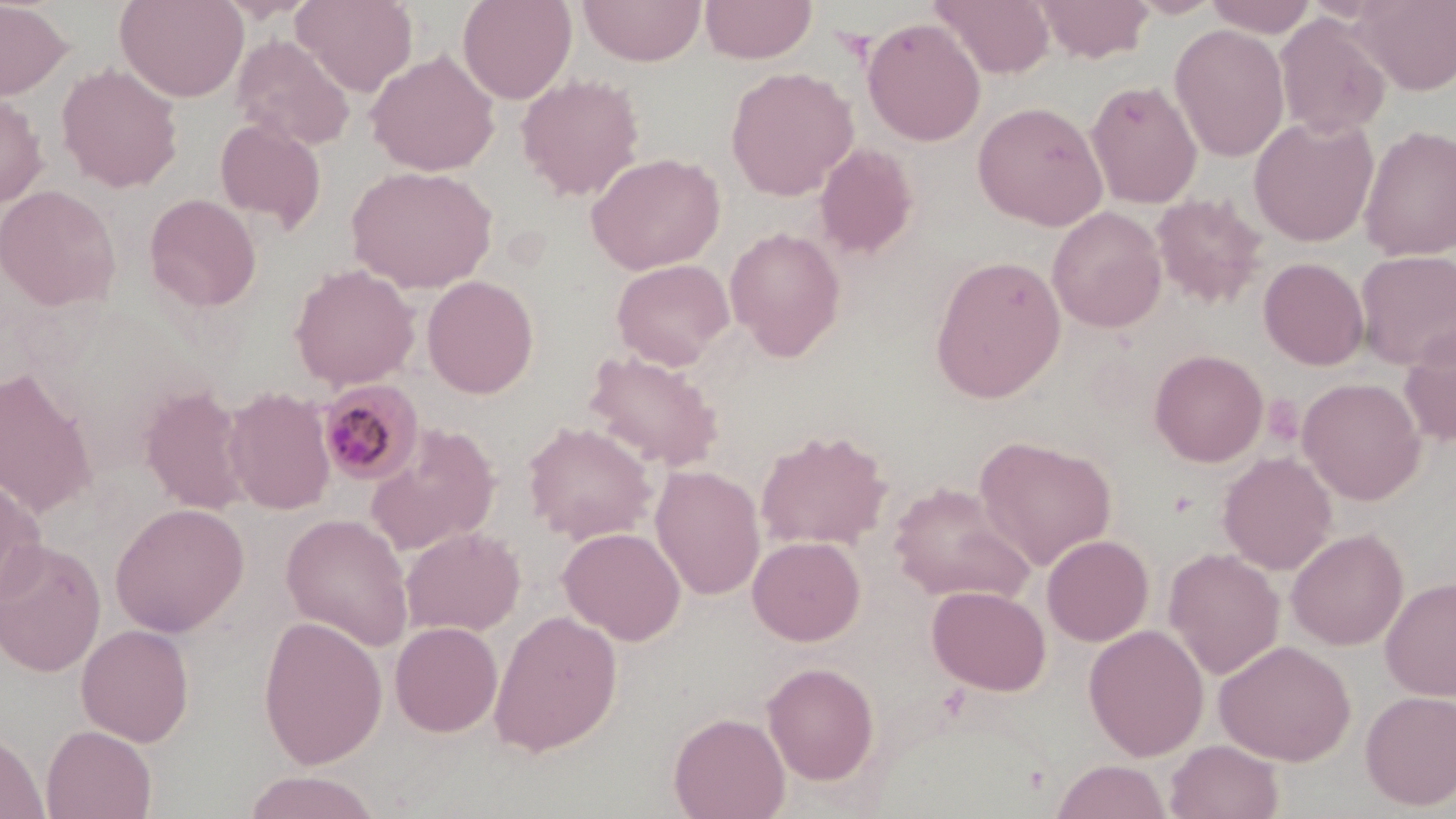 Approximate bounding boxes as (x1, y1, x2, y2) in pixels. Uninfected red blood cell locations: (0, 0, 75, 101), (115, 0, 248, 102), (291, 0, 418, 95), (457, 0, 576, 104), (699, 0, 817, 64), (931, 0, 1055, 79), (1034, 0, 1155, 63), (1127, 0, 1226, 19), (1203, 0, 1319, 37), (1353, 0, 1456, 95), (578, 1, 707, 66), (1274, 14, 1391, 139), (862, 17, 986, 147), (1169, 24, 1290, 162), (231, 34, 355, 151), (365, 49, 500, 176), (56, 63, 183, 193), (726, 66, 858, 200), (516, 74, 645, 200), (1086, 79, 1202, 208), (0, 91, 49, 209), (972, 101, 1108, 231), (1248, 114, 1379, 247), (215, 118, 326, 231), (1359, 124, 1456, 261), (815, 142, 919, 259), (586, 152, 725, 274), (346, 165, 498, 293), (0, 184, 122, 311), (1151, 192, 1268, 310), (144, 193, 262, 312), (1048, 206, 1167, 332), (724, 227, 846, 360), (1355, 250, 1456, 370), (930, 254, 1067, 403), (1258, 257, 1370, 371), (611, 258, 734, 369), (289, 264, 421, 391), (422, 275, 539, 399), (1399, 324, 1456, 447), (1149, 349, 1268, 467), (583, 351, 724, 471), (0, 367, 98, 517), (1297, 377, 1426, 505), (140, 386, 251, 514), (223, 386, 336, 515), (523, 422, 657, 543), (364, 423, 501, 555), (755, 429, 892, 551), (974, 435, 1117, 570), (1218, 452, 1337, 575), (650, 465, 765, 600), (0, 469, 46, 607), (888, 482, 1034, 606), (110, 502, 249, 637), (281, 512, 414, 651), (558, 526, 686, 645), (400, 527, 525, 636), (1286, 527, 1409, 651), (1042, 534, 1154, 646), (747, 535, 866, 646), (0, 540, 106, 677), (1164, 548, 1285, 679), (1380, 577, 1456, 701), (927, 585, 1050, 695), (488, 610, 623, 756), (258, 615, 387, 769), (389, 621, 503, 737), (76, 623, 194, 746), (1083, 624, 1209, 761), (1215, 640, 1356, 764), (762, 661, 879, 785), (1360, 690, 1456, 810), (669, 712, 791, 819), (41, 725, 157, 819), (0, 729, 48, 819), (1165, 739, 1284, 819), (1051, 759, 1172, 819), (242, 771, 381, 818). Plasmodium malariae-infected red blood cell locations: (316, 380, 425, 487). Slide-level diagnosis: Plasmodium malariae. Thin blood film. Captured at 1000x magnification. Image is 1456×819 pixels. One field of a larger specimen. May-Grünwald-Giemsa stain. Light microscopy.